Comment on the morphology of the red blood cells.
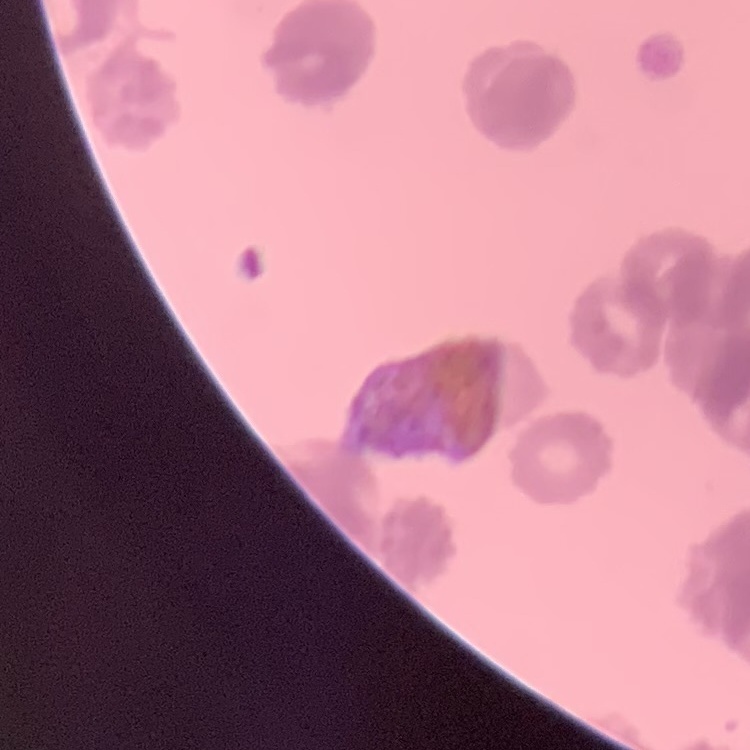
They show rouleaux formation.

Field's or Giemsa stain. Square crop of a larger photomicrograph. Thin blood film.